Describe the morphology of the erythrocytes.
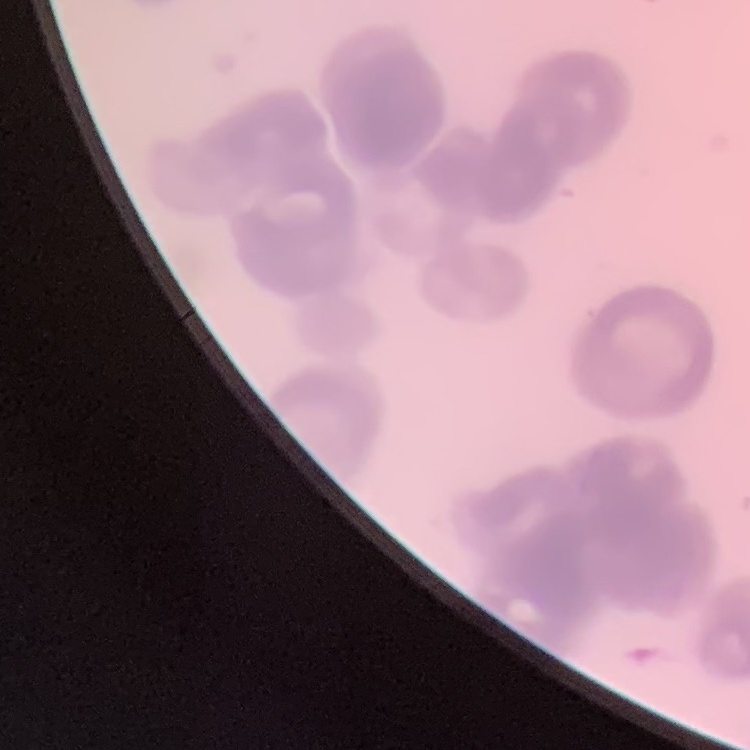
They show rouleaux formation.

One tile cut from a larger photomicrograph. Thin peripheral smear. Field's or Giemsa stain.